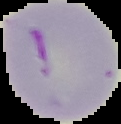
Summary:
  - Image size: 121×124 pixels
  - Image type: cell region segmented out of the field of view; surrounding area masked to black
  - Malaria status: parasitized
  - Preparation: thin blood film